Locate every P. falciparum parasite and identify its life-cycle stage.
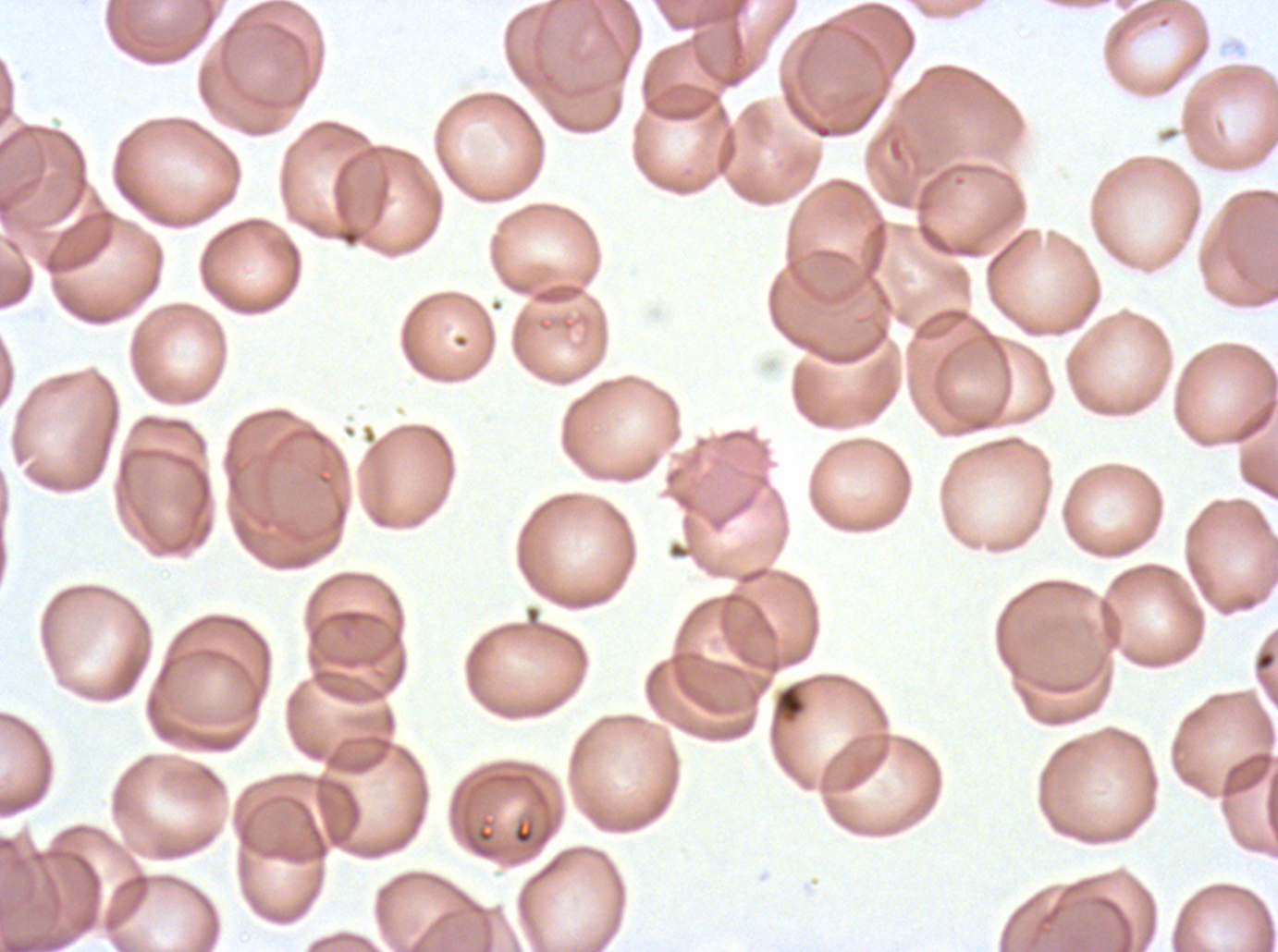
No rings, late-ring/early-trophozoite forms, mid trophozoites, late trophozoites, early schizonts, late schizonts, segmenters, or gametocytes observed.

Approximate bounding boxes as {x1, y1, x2, y2} in pixels.
Summary:
  - Debris locations: {1253, 647, 1277, 687}, {770, 679, 808, 728}
  - Specimen: P. falciparum from a patient in The Gambia, cultured ex vivo for 24 to 48 hours
  - Image size: 1278×952 pixels
  - Preparation: thin blood film
  - Field of view: sub-image separated from a larger composite
  - Stain: Giemsa